Give the extent of all Plasmodium ovale-infected red blood cells.
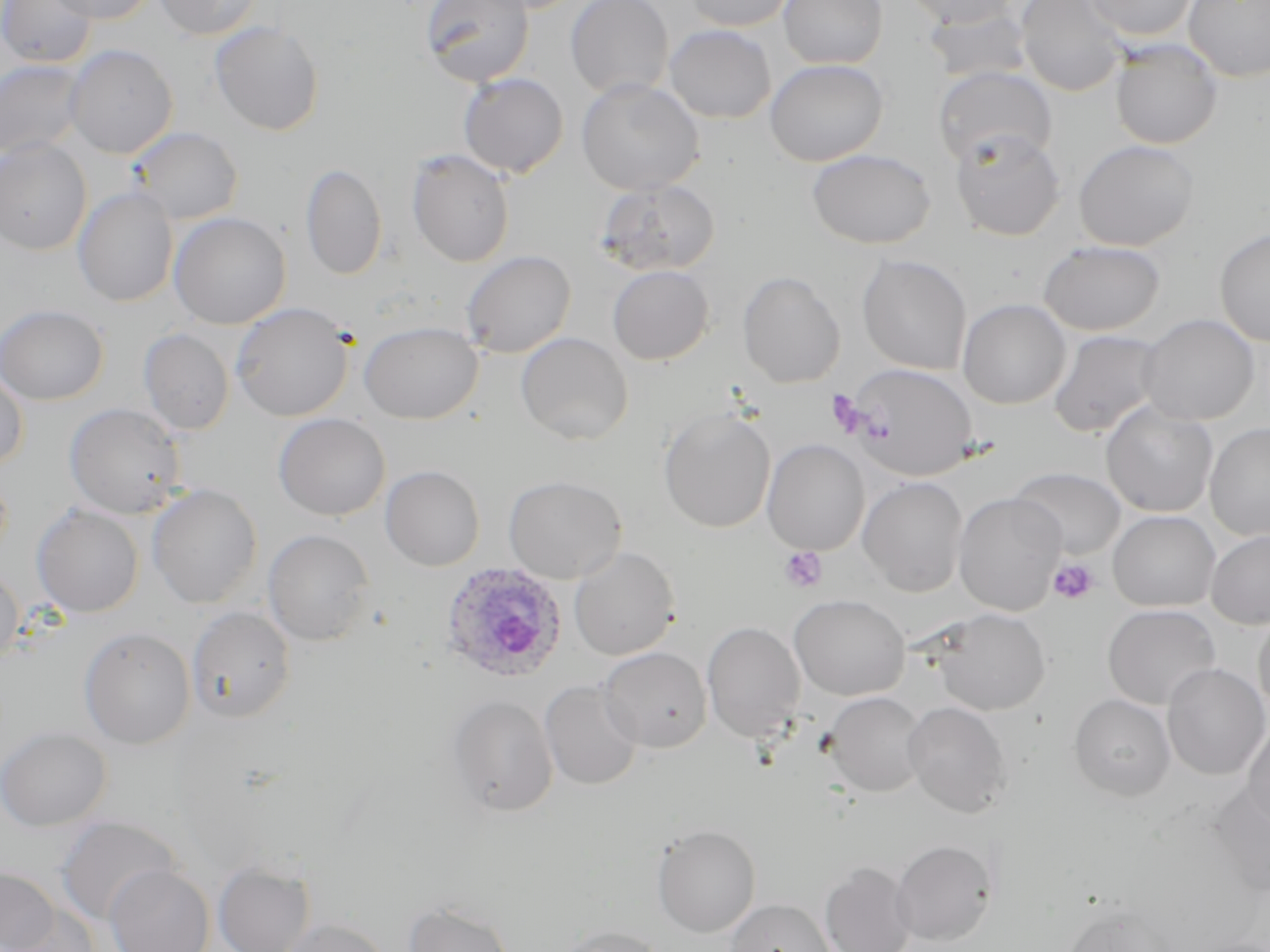

Approximate bounding boxes as named x1/y1/x2/y2 corners in pixels.
Plasmodium ovale-infected red blood cells: (x1=439, y1=562, x2=568, y2=685).

Platelet locations: (x1=826, y1=389, x2=870, y2=437), (x1=779, y1=546, x2=828, y2=592), (x1=1048, y1=557, x2=1099, y2=605). Uninfected red blood cell locations: (x1=0, y1=0, x2=96, y2=68), (x1=46, y1=0, x2=158, y2=24), (x1=154, y1=0, x2=261, y2=39), (x1=420, y1=0, x2=534, y2=87), (x1=565, y1=0, x2=674, y2=99), (x1=682, y1=0, x2=795, y2=31), (x1=778, y1=0, x2=888, y2=69), (x1=902, y1=0, x2=1017, y2=29), (x1=1015, y1=0, x2=1129, y2=96), (x1=1083, y1=0, x2=1197, y2=41), (x1=1184, y1=0, x2=1270, y2=82), (x1=924, y1=7, x2=1034, y2=85), (x1=209, y1=21, x2=325, y2=136), (x1=664, y1=24, x2=776, y2=123), (x1=1110, y1=40, x2=1222, y2=149), (x1=65, y1=45, x2=178, y2=159), (x1=0, y1=59, x2=87, y2=160), (x1=764, y1=59, x2=888, y2=166), (x1=934, y1=66, x2=1057, y2=168), (x1=458, y1=73, x2=569, y2=178), (x1=576, y1=78, x2=704, y2=195), (x1=127, y1=126, x2=244, y2=224), (x1=950, y1=129, x2=1066, y2=241), (x1=0, y1=139, x2=92, y2=255), (x1=1073, y1=139, x2=1200, y2=251), (x1=807, y1=148, x2=936, y2=249), (x1=406, y1=150, x2=515, y2=267), (x1=300, y1=162, x2=387, y2=280), (x1=596, y1=178, x2=721, y2=277), (x1=73, y1=187, x2=179, y2=307), (x1=169, y1=212, x2=291, y2=329), (x1=1214, y1=228, x2=1270, y2=347), (x1=1038, y1=240, x2=1165, y2=336), (x1=460, y1=250, x2=576, y2=358), (x1=857, y1=254, x2=972, y2=374), (x1=607, y1=265, x2=715, y2=365), (x1=737, y1=271, x2=845, y2=388), (x1=957, y1=298, x2=1071, y2=409), (x1=231, y1=302, x2=353, y2=421), (x1=0, y1=304, x2=109, y2=405), (x1=1138, y1=313, x2=1260, y2=425), (x1=358, y1=321, x2=484, y2=424), (x1=138, y1=328, x2=234, y2=435), (x1=1047, y1=329, x2=1165, y2=438), (x1=516, y1=332, x2=633, y2=445), (x1=843, y1=362, x2=980, y2=480), (x1=0, y1=369, x2=28, y2=470), (x1=1100, y1=402, x2=1218, y2=517), (x1=64, y1=403, x2=186, y2=519), (x1=658, y1=408, x2=776, y2=533), (x1=273, y1=413, x2=390, y2=521), (x1=1205, y1=422, x2=1270, y2=541), (x1=763, y1=439, x2=869, y2=556), (x1=381, y1=465, x2=485, y2=570), (x1=1011, y1=467, x2=1126, y2=560), (x1=503, y1=475, x2=627, y2=583), (x1=858, y1=477, x2=968, y2=596), (x1=147, y1=483, x2=263, y2=609), (x1=953, y1=492, x2=1066, y2=615), (x1=32, y1=505, x2=144, y2=618), (x1=1107, y1=510, x2=1220, y2=611), (x1=262, y1=529, x2=375, y2=646), (x1=1206, y1=530, x2=1270, y2=629), (x1=569, y1=546, x2=680, y2=660), (x1=0, y1=564, x2=23, y2=665), (x1=790, y1=593, x2=910, y2=700), (x1=1102, y1=604, x2=1221, y2=710), (x1=186, y1=606, x2=296, y2=722), (x1=930, y1=608, x2=1051, y2=715), (x1=1253, y1=608, x2=1270, y2=717), (x1=702, y1=621, x2=806, y2=743), (x1=79, y1=627, x2=196, y2=748), (x1=599, y1=647, x2=712, y2=752), (x1=1162, y1=663, x2=1270, y2=779), (x1=540, y1=680, x2=643, y2=790), (x1=823, y1=691, x2=928, y2=797), (x1=1069, y1=694, x2=1176, y2=802), (x1=447, y1=695, x2=559, y2=816), (x1=902, y1=701, x2=1012, y2=817), (x1=1242, y1=719, x2=1270, y2=829), (x1=0, y1=726, x2=111, y2=831), (x1=1208, y1=782, x2=1270, y2=898), (x1=56, y1=816, x2=181, y2=925), (x1=652, y1=824, x2=761, y2=937), (x1=891, y1=839, x2=996, y2=945), (x1=213, y1=860, x2=315, y2=952), (x1=820, y1=861, x2=917, y2=952), (x1=104, y1=863, x2=214, y2=952), (x1=0, y1=867, x2=60, y2=951), (x1=724, y1=898, x2=836, y2=952), (x1=403, y1=901, x2=514, y2=952), (x1=1062, y1=902, x2=1176, y2=952), (x1=4, y1=904, x2=99, y2=952), (x1=275, y1=917, x2=391, y2=952), (x1=554, y1=926, x2=667, y2=952). Slide-level diagnosis: Plasmodium ovale. May-Grünwald-Giemsa stain. Image is 1270×952 pixels. Light microscopy. Thin blood film. One field of a larger specimen. 1000x magnification.